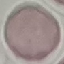 Malaria status: uninfected. Cell patch, automatically extracted from a larger field of view and resized to 64 × 64 pixels. Photographed with a smartphone camera at the microscope eyepiece. Thin blood film. Giemsa stain.